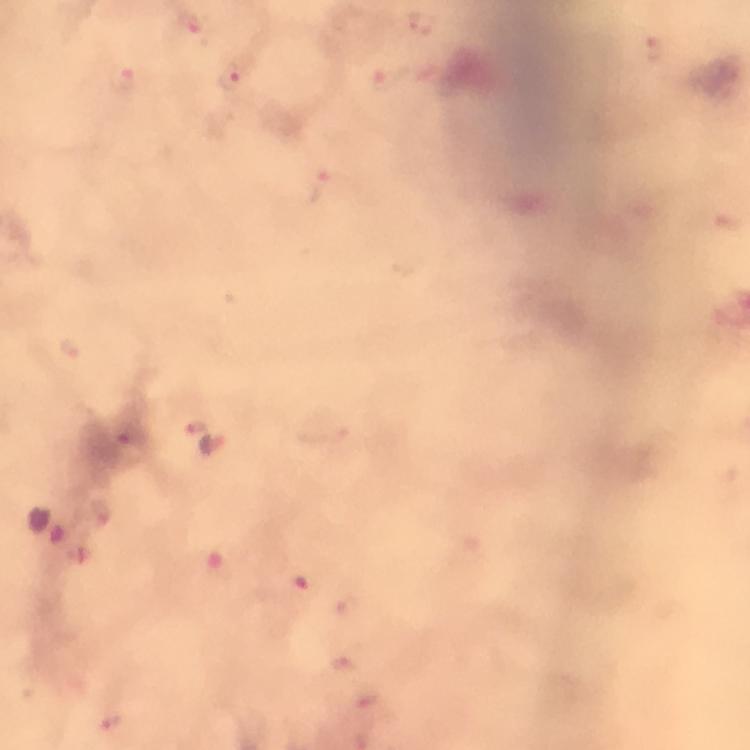

Approximate centers as {x, y} in pixels.
Summary:
  - Malaria parasite locations: {420, 20}, {190, 22}, {656, 49}, {229, 78}, {121, 79}, {384, 80}, {317, 188}, {70, 348}, {195, 428}, {127, 431}, {99, 510}
  - Capture: smartphone mounted on the microscope
  - Context: from a diagnostic examination for malaria
  - Stain: Giemsa
  - Preparation: thick blood film
  - Image size: 750×750 pixels
  - Cropped from: one field of view
  - Magnification: 100x
  - Immersion oil: applied